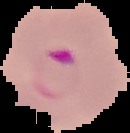 From a thin blood smear. The area outside the segmented cell region is set to black. Malaria status: parasitized. Image is 130×133 pixels.